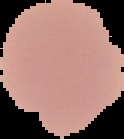
preparation = thin blood smear
result = no Plasmodium parasites detected
image size = 124×139 pixels
image type = segmented cell region with the area outside set to black